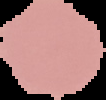 Image is 106×100 pixels. Segmented cell region on a black background. From a thin blood smear. Result: no Plasmodium parasites detected.